Locate platelets.
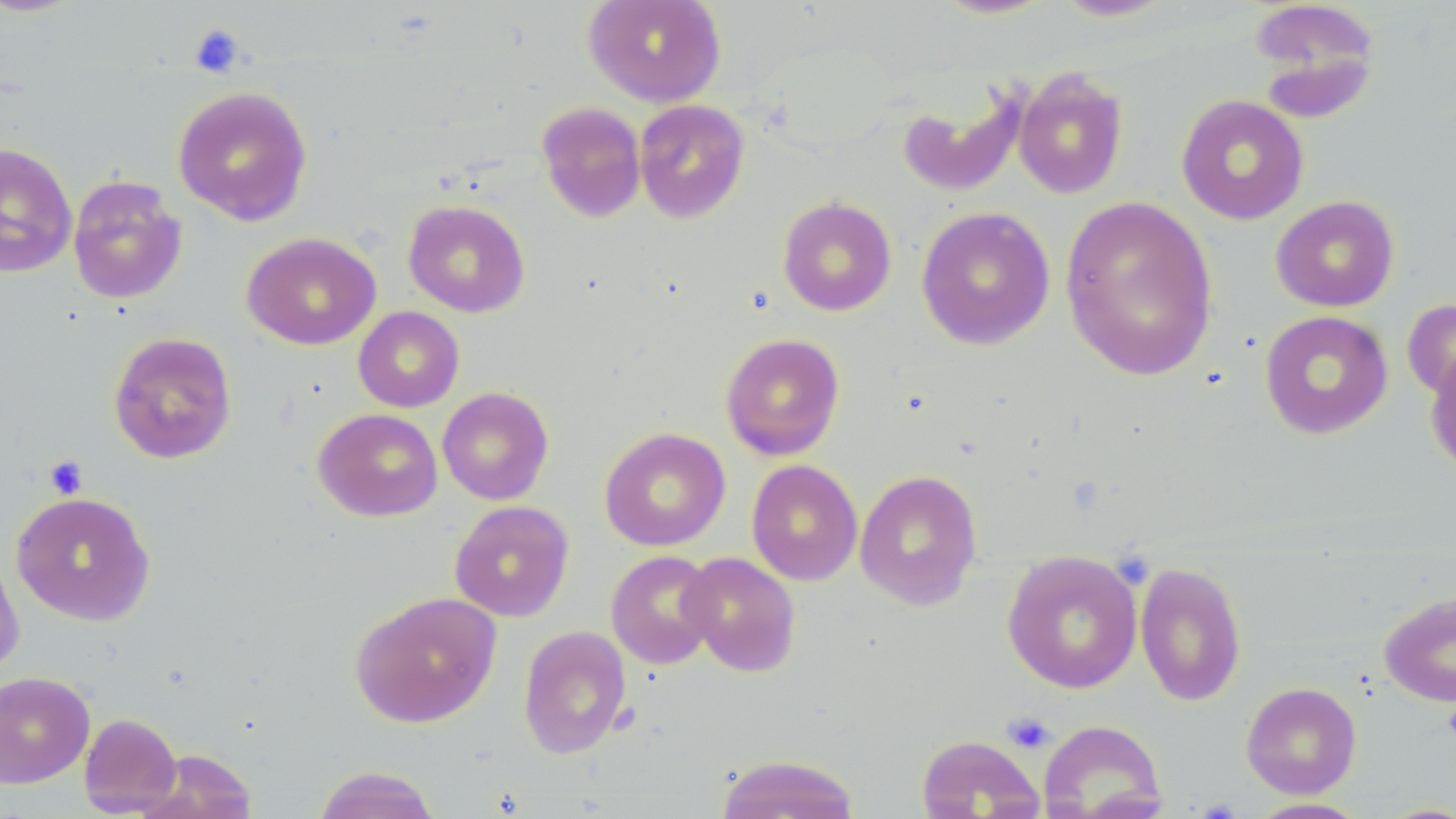
Approximate bounding boxes as (x1, y1, x2, y2) in pixels.
Platelets: (188, 24, 246, 78), (44, 457, 88, 498), (1002, 712, 1056, 753).

slide-level diagnosis = no evidence of blood parasites
preparation = thin blood film
field of view = single
stain = May-Grünwald-Giemsa
image size = 1456×819 pixels
magnification = 1000x
uninfected red blood cell locations = approximate bounding boxes as (x1, y1, x2, y2) in pixels: (583, 0, 726, 107), (931, 0, 1058, 20), (1052, 0, 1177, 22), (1248, 0, 1382, 118), (1012, 67, 1129, 200), (172, 85, 313, 226), (896, 85, 1026, 198), (1176, 94, 1309, 225), (633, 99, 750, 224), (536, 101, 646, 223), (0, 143, 77, 278), (68, 176, 187, 304), (1058, 194, 1219, 381), (1271, 194, 1399, 312), (777, 196, 897, 316), (403, 199, 530, 317), (916, 206, 1055, 350), (241, 231, 381, 350), (1402, 296, 1456, 405), (353, 306, 464, 412), (1259, 310, 1394, 440), (108, 332, 237, 464), (720, 333, 845, 460), (1424, 338, 1456, 476), (437, 386, 554, 505), (312, 407, 444, 522), (599, 427, 731, 551), (746, 459, 863, 586), (855, 468, 983, 610), (11, 491, 155, 626), (449, 500, 574, 622), (0, 544, 25, 677), (605, 550, 721, 669), (1001, 550, 1144, 694), (680, 551, 802, 677), (1134, 561, 1247, 707), (350, 591, 501, 728), (1379, 591, 1456, 707), (517, 625, 632, 759), (0, 671, 95, 788), (1240, 681, 1362, 799), (79, 713, 182, 816), (1038, 719, 1167, 819), (915, 734, 1045, 818), (139, 748, 257, 819), (713, 753, 862, 818), (311, 765, 443, 819), (1245, 798, 1373, 818)
modality = optical microscopy